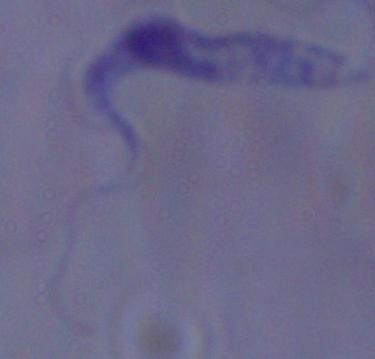

identification = trypanosome
magnification = 1000x
modality = micrograph